Locate every Plasmodium falciparum-infected red blood cell.
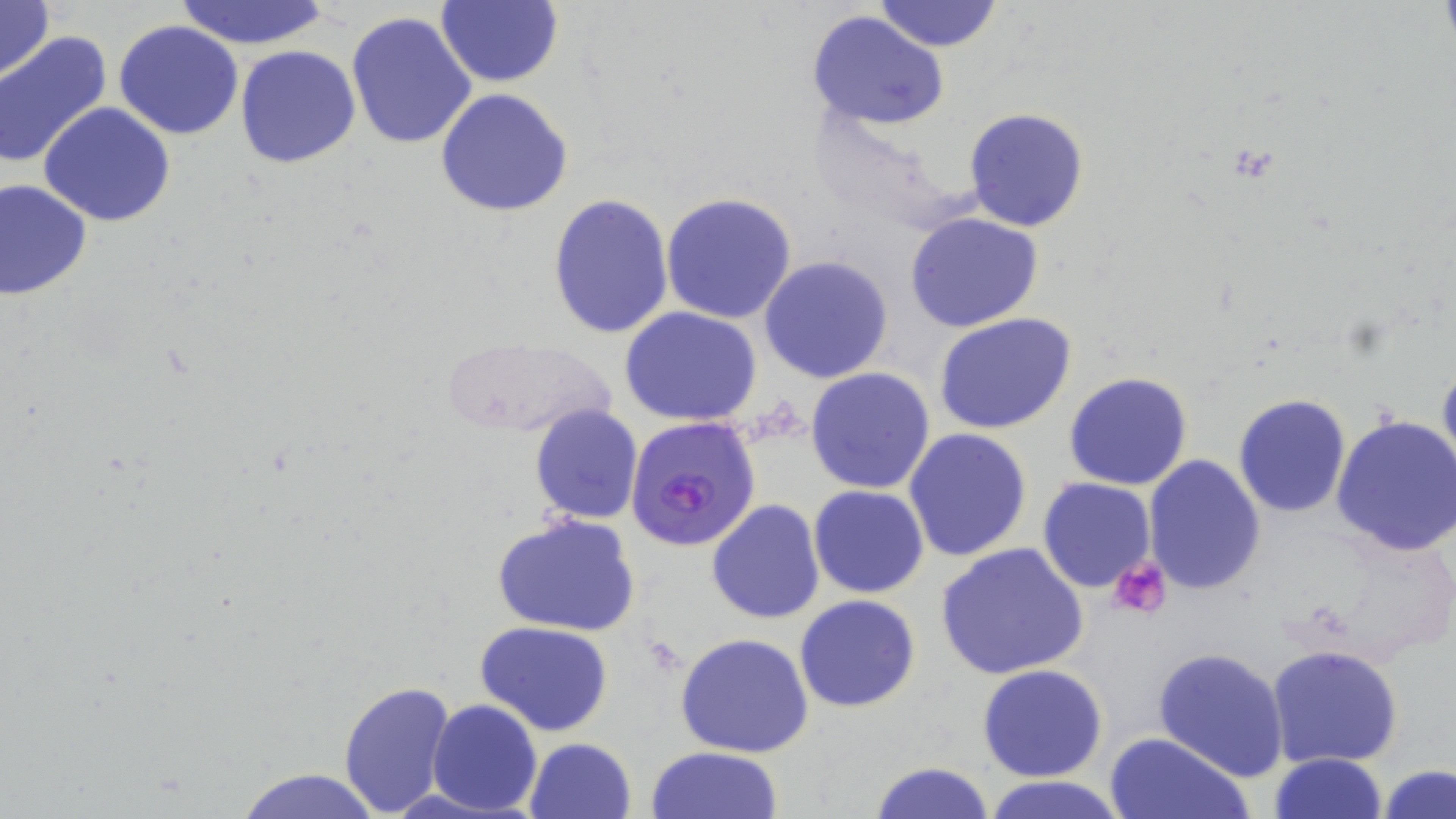

Approximate bounding boxes as (x1,y1)-(x2,y2) corner pairs in pixels.
Plasmodium falciparum-infected red blood cells: (624,416)-(761,553).

Uninfected red blood cell locations: (0,0)-(53,82), (436,0)-(563,88), (873,0)-(1004,52), (173,1)-(331,49), (346,10)-(478,150), (807,11)-(951,130), (113,19)-(245,140), (0,32)-(112,169), (234,44)-(362,168), (435,87)-(575,217), (39,102)-(178,227), (964,108)-(1089,230), (0,178)-(93,301), (662,192)-(798,324), (548,194)-(675,342), (905,211)-(1043,332), (759,256)-(894,384), (620,307)-(765,426), (933,312)-(1077,434), (439,334)-(615,439), (1436,359)-(1456,485), (805,367)-(936,495), (1064,372)-(1194,491), (1233,394)-(1353,518), (530,404)-(644,525), (1332,415)-(1456,558), (904,428)-(1033,563), (1143,455)-(1267,595), (1037,478)-(1156,593), (809,485)-(929,599), (707,500)-(825,624), (492,512)-(641,637), (935,543)-(1090,683), (795,594)-(922,712), (475,621)-(617,736), (675,633)-(815,757), (1267,644)-(1402,768), (1152,646)-(1289,781), (976,664)-(1107,782), (337,679)-(457,818), (427,699)-(543,816), (1105,730)-(1253,819), (523,737)-(637,819), (647,745)-(784,819), (1268,752)-(1387,819), (866,760)-(994,819), (1379,765)-(1456,819), (233,766)-(384,819), (981,774)-(1129,819). Platelet locations: (1109,555)-(1170,618). Slide-level diagnosis: Plasmodium falciparum. Optical microscopy. May-Grünwald-Giemsa-stained preparation. Single field of view. Image is 1456×819 pixels. Captured at 1000x magnification. Thin blood smear.